Point out each Plasmodium parasite.
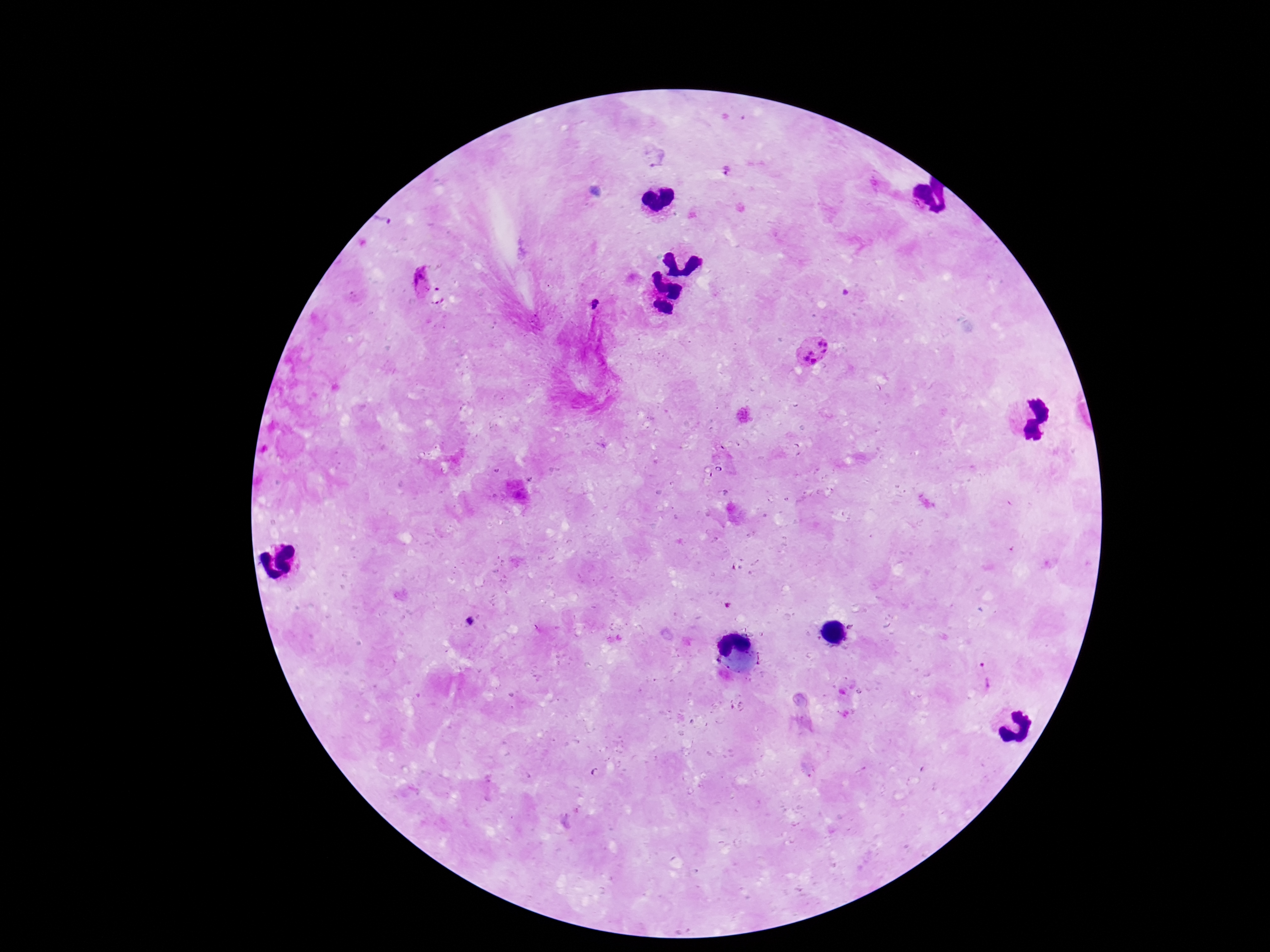
Approximate centers as (x, y) in pixels.
Plasmodium parasites: (725, 172), (421, 284), (593, 306), (813, 350), (471, 621), (988, 675).

patient malaria status = infected
capture = smartphone camera through the microscope eyepiece
field of view = single
image size = 1270×952 pixels
magnification = 100x
preparation = thick blood smear
stain = Giemsa